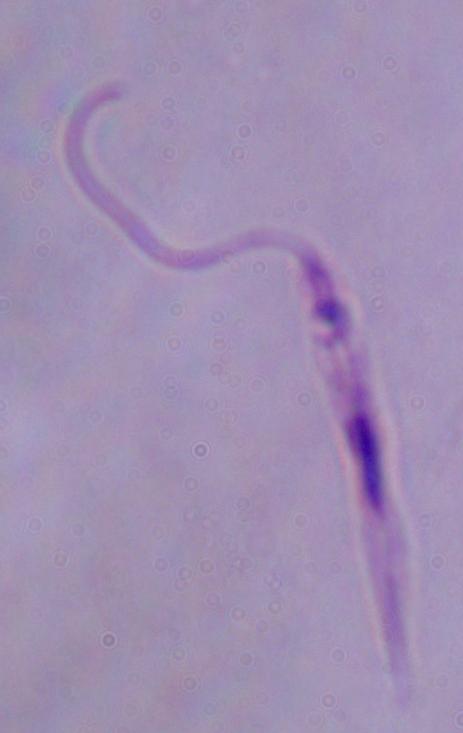
Summary:
  - Identification: Leishmania
  - Magnification: 1000x
  - Modality: micrograph